Assess for malaria.
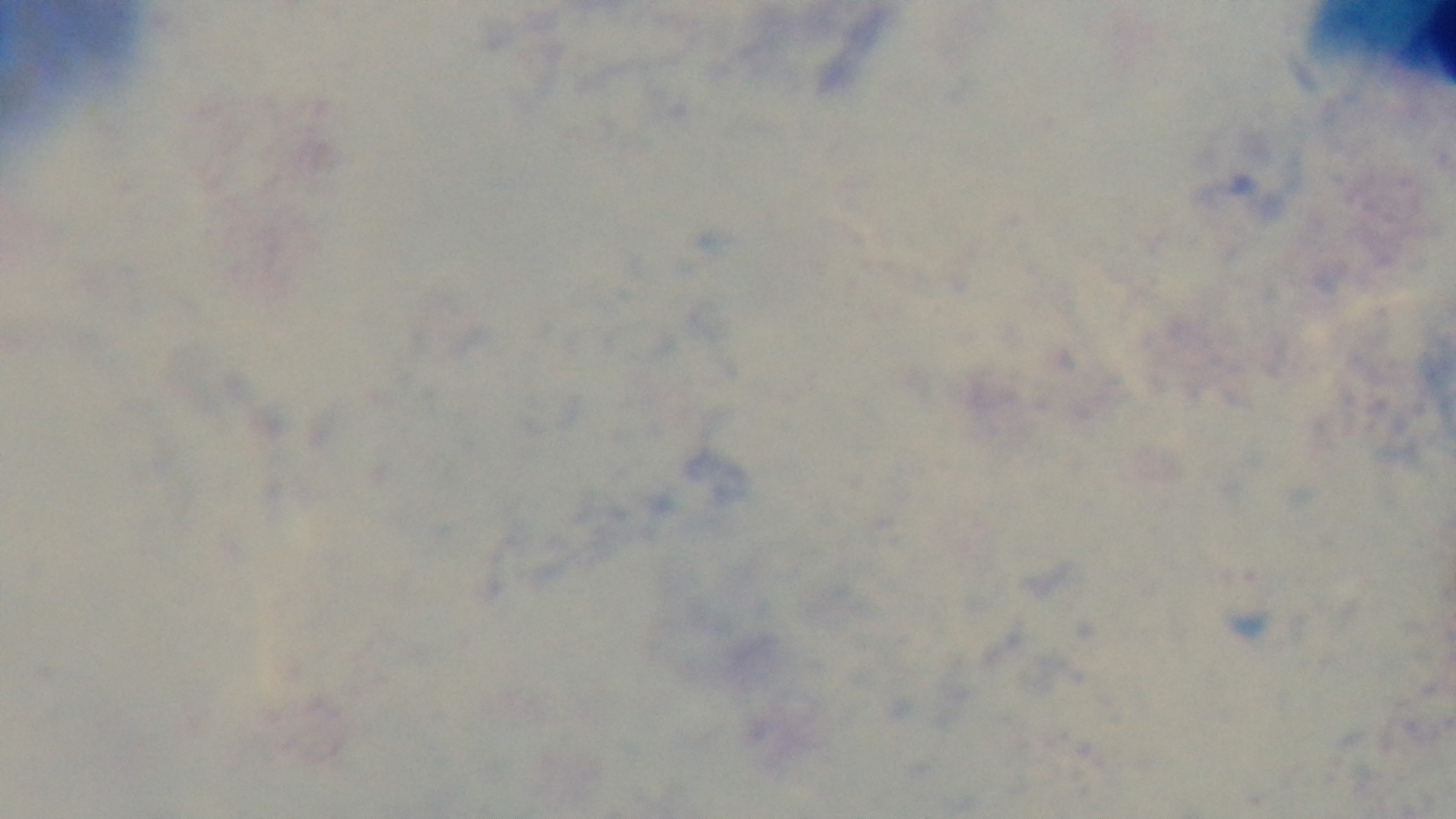
Uninfected.

modality = light microscopy
preparation = thick blood film
capture = mounted 4K digital camera
field of view = one from the slide
objective = 100x oil immersion
stain = Giemsa